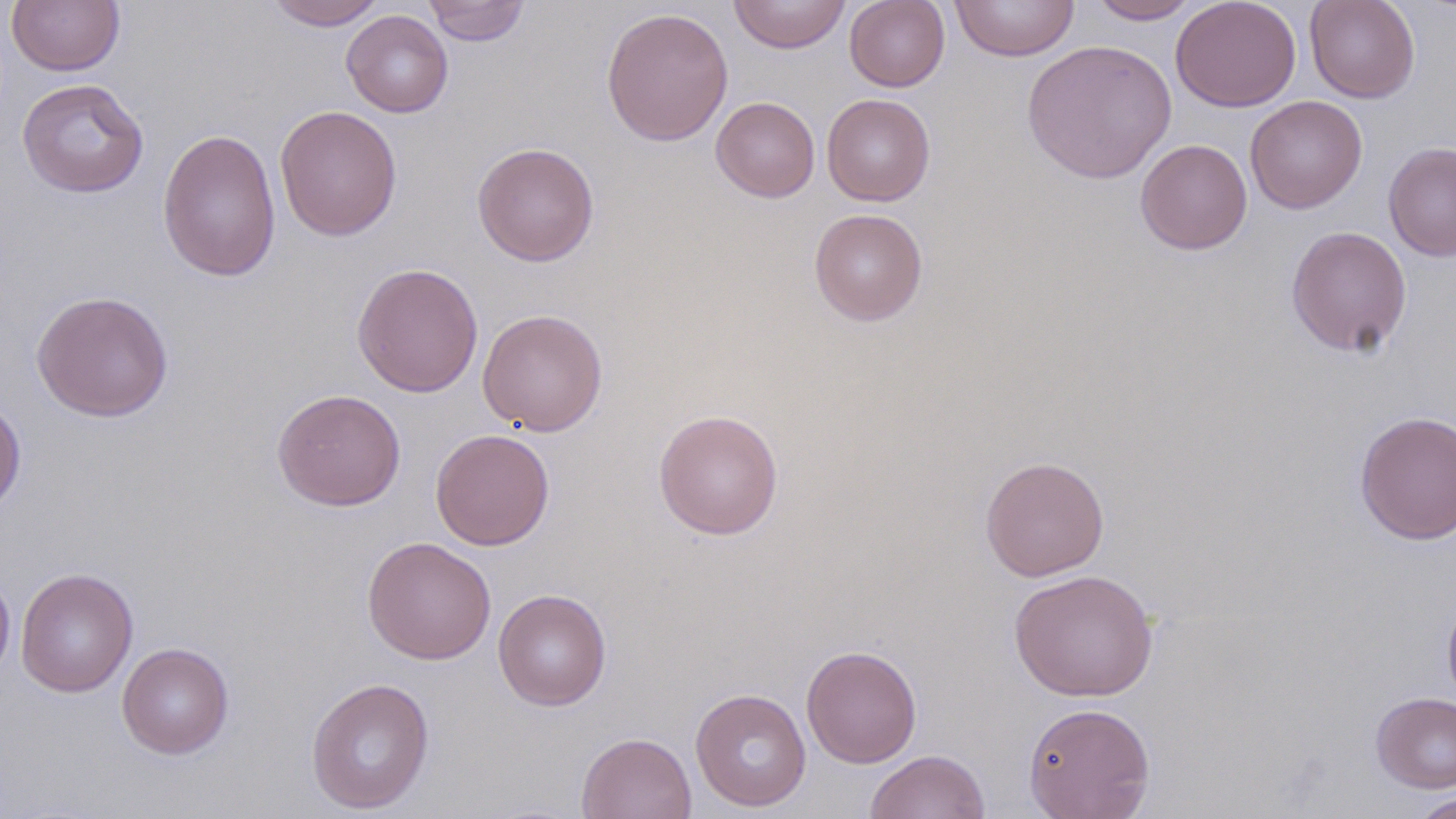

Summary:
  - Coordinate format: approximate bounding boxes as (x1, y1, x2, y2) in pixels
  - Uninfected red blood cell locations: (265, 0, 387, 30), (421, 0, 531, 46), (729, 0, 851, 54), (844, 0, 950, 92), (950, 0, 1080, 62), (1087, 0, 1202, 24), (1171, 0, 1302, 113), (1304, 0, 1421, 103), (7, 1, 125, 75), (601, 7, 734, 146), (341, 10, 453, 117), (1022, 39, 1177, 184), (16, 78, 149, 198), (821, 93, 935, 206), (711, 96, 820, 203), (1245, 96, 1367, 214), (275, 105, 402, 241), (157, 128, 282, 283), (1135, 139, 1252, 255), (472, 141, 600, 266), (1383, 141, 1456, 262), (809, 208, 928, 326), (1285, 226, 1413, 357), (351, 262, 484, 398), (31, 290, 174, 423), (477, 308, 608, 436), (271, 388, 406, 511), (0, 396, 27, 518), (653, 409, 784, 540), (1354, 410, 1456, 545), (429, 429, 555, 550), (980, 455, 1110, 581), (361, 536, 497, 664), (16, 567, 138, 697), (0, 568, 16, 685), (1008, 568, 1159, 702), (493, 588, 612, 711), (1442, 590, 1456, 710), (116, 642, 234, 759), (801, 645, 922, 768), (305, 676, 435, 815), (690, 687, 812, 812), (1371, 692, 1456, 792), (1023, 702, 1156, 818), (576, 731, 697, 819), (864, 750, 991, 819), (1410, 793, 1456, 818)
  - Slide-level diagnosis: no evidence of blood parasites
  - Magnification: 1000x
  - Stain: May-Grünwald-Giemsa
  - Modality: light microscopy
  - Preparation: thin blood film
  - Image size: 1456×819 pixels
  - Field of view: single